Outline each Plasmodium vivax-infected red blood cell.
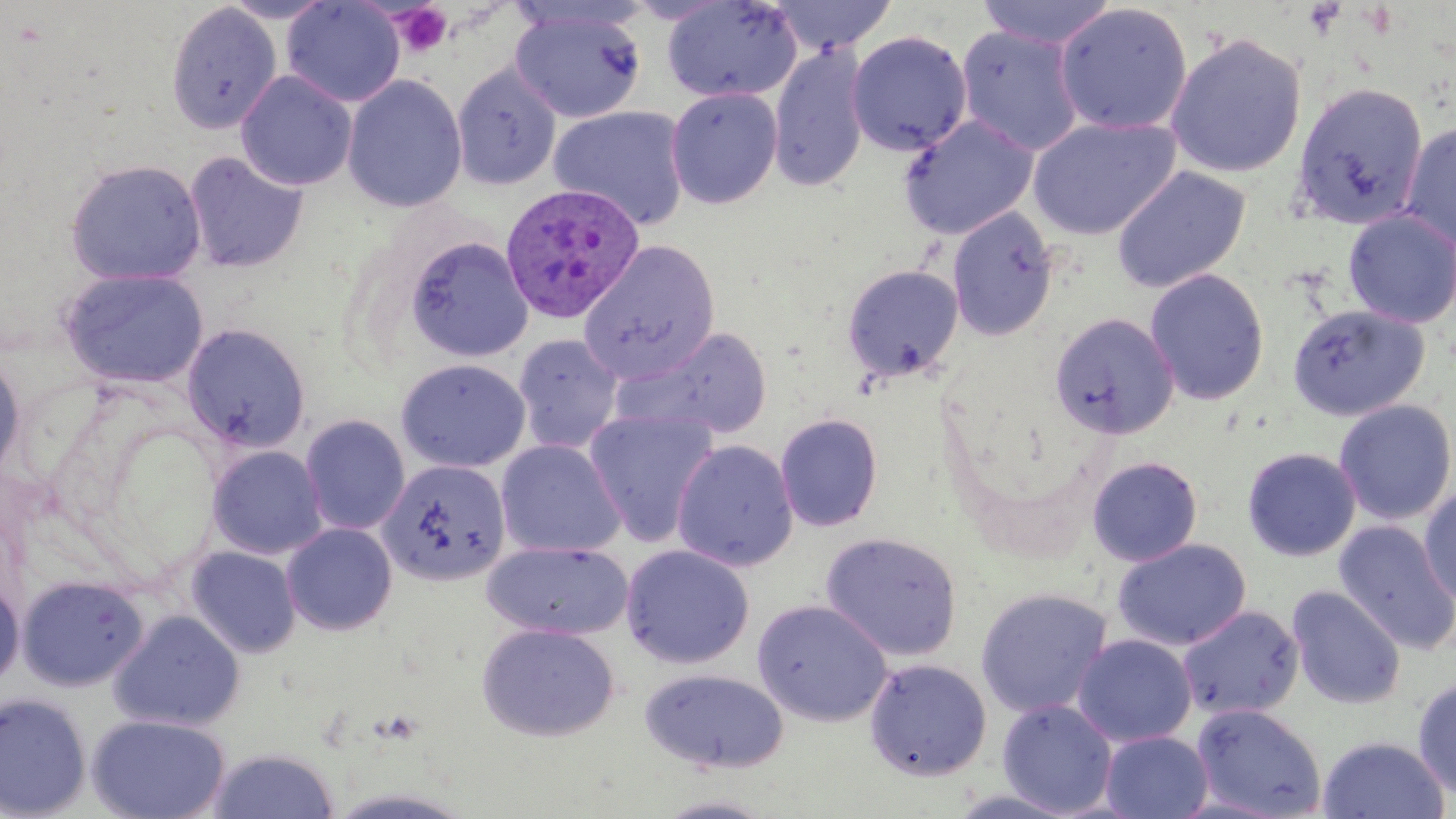
Approximate bounding boxes as [x1, y1, x2, y2] in pixels.
Plasmodium vivax-infected red blood cells: [499, 183, 646, 324].

Summary:
  - Uninfected red blood cell locations: [219, 0, 337, 23], [282, 0, 405, 108], [661, 0, 803, 103], [769, 0, 898, 55], [976, 0, 1118, 49], [166, 2, 282, 134], [1054, 3, 1193, 135], [509, 6, 647, 124], [955, 24, 1085, 157], [846, 31, 972, 156], [1164, 32, 1307, 178], [768, 44, 870, 193], [450, 62, 562, 191], [235, 70, 358, 191], [342, 74, 467, 213], [1291, 82, 1428, 230], [665, 86, 783, 209], [548, 104, 691, 231], [897, 114, 1038, 239], [1028, 117, 1180, 239], [1399, 121, 1456, 251], [183, 152, 309, 273], [64, 158, 207, 286], [1111, 166, 1251, 294], [947, 207, 1059, 340], [1343, 209, 1456, 328], [404, 236, 533, 362], [578, 240, 719, 384], [841, 264, 965, 385], [61, 267, 209, 390], [1145, 269, 1269, 406], [1287, 303, 1429, 421], [1050, 312, 1179, 438], [184, 323, 311, 452], [616, 325, 774, 441], [513, 333, 624, 454], [0, 352, 26, 484], [396, 358, 531, 473], [1334, 399, 1456, 525], [584, 408, 719, 547], [775, 413, 883, 532], [300, 414, 411, 535], [495, 439, 626, 558], [672, 439, 799, 571], [207, 445, 328, 560], [1242, 447, 1361, 561], [1086, 456, 1203, 566], [378, 459, 511, 586], [1418, 483, 1456, 607], [1333, 520, 1456, 654], [282, 522, 397, 636], [820, 532, 963, 661], [1113, 538, 1252, 651], [483, 540, 634, 640], [619, 544, 755, 669], [186, 546, 301, 658], [18, 575, 148, 691], [0, 580, 24, 689], [1287, 585, 1405, 709], [975, 587, 1113, 719], [752, 598, 892, 727], [1177, 605, 1304, 722], [108, 609, 246, 731], [476, 622, 619, 742], [1072, 634, 1197, 747], [864, 658, 992, 781], [639, 668, 789, 773], [1412, 676, 1456, 802], [0, 692, 92, 818], [997, 699, 1118, 816], [1191, 703, 1326, 819], [87, 713, 231, 819], [1100, 730, 1214, 819], [1317, 735, 1450, 818], [207, 747, 339, 818], [945, 786, 1079, 817], [653, 794, 779, 818]
  - Platelet locations: [392, 3, 453, 57]
  - Slide-level diagnosis: Plasmodium vivax
  - Magnification: 1000x
  - Stain: May-Grünwald-Giemsa
  - Field of view: single
  - Modality: light microscopy
  - Preparation: thin blood smear
  - Image size: 1456×819 pixels